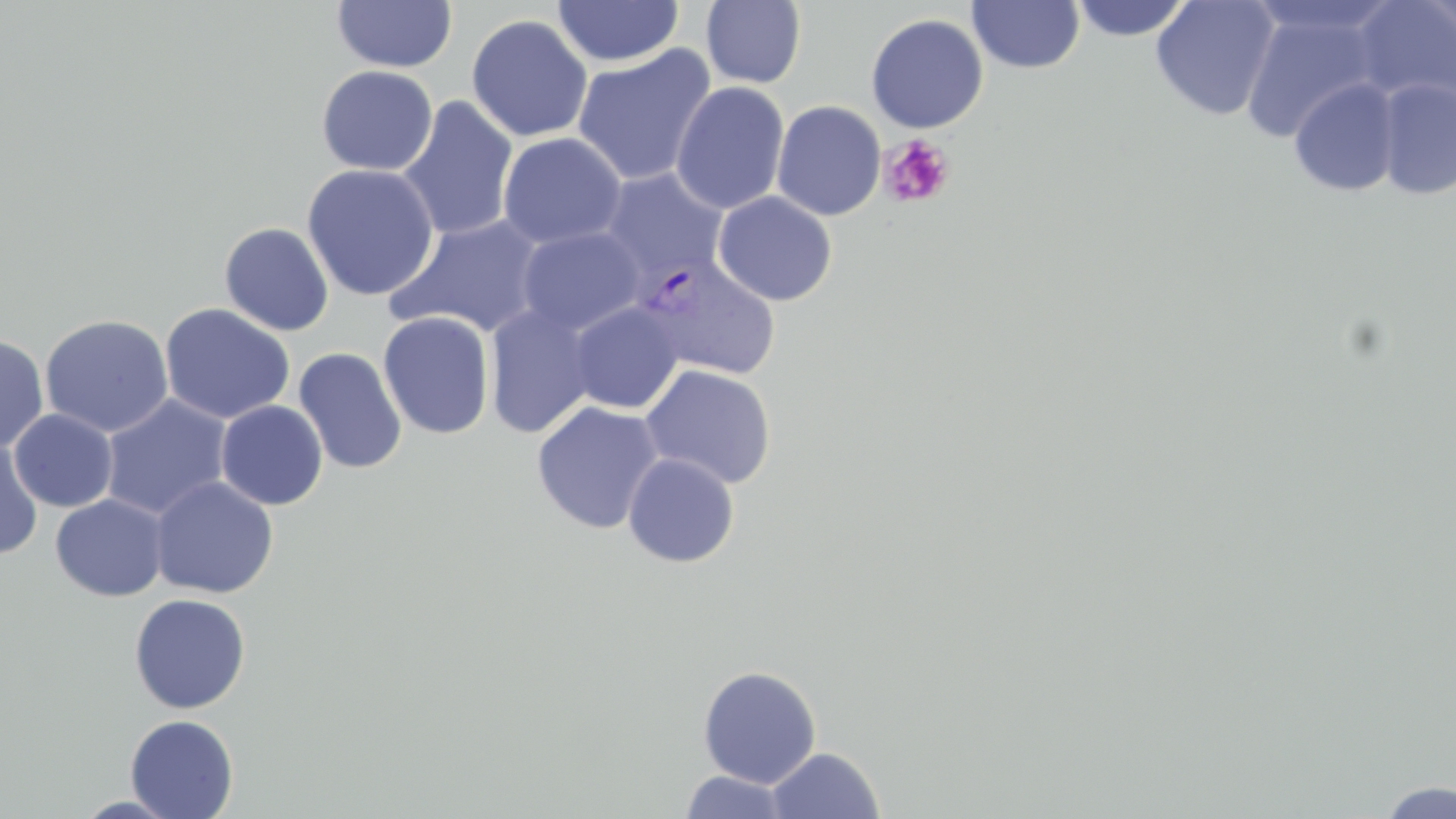

Summary:
  - Coordinate format: approximate bounding boxes as [x1, y1, x2, y2] in pixels
  - Uninfected red blood cell locations: [331, 0, 457, 73], [1069, 0, 1193, 42], [1151, 0, 1280, 121], [1351, 0, 1456, 113], [552, 1, 684, 68], [701, 1, 806, 89], [967, 1, 1085, 75], [1239, 6, 1387, 142], [866, 13, 989, 134], [466, 14, 593, 143], [572, 44, 718, 186], [316, 65, 438, 176], [1288, 77, 1401, 199], [1375, 77, 1456, 200], [670, 81, 790, 215], [396, 96, 519, 242], [772, 100, 886, 221], [498, 132, 627, 250], [301, 163, 440, 301], [598, 168, 729, 287], [712, 191, 838, 306], [387, 214, 547, 338], [219, 222, 334, 336], [516, 227, 646, 338], [567, 302, 684, 414], [159, 303, 295, 425], [484, 303, 598, 439], [378, 311, 495, 440], [39, 313, 175, 438], [0, 336, 49, 454], [294, 347, 407, 474], [640, 364, 777, 490], [100, 395, 233, 521], [215, 400, 328, 510], [531, 401, 666, 535], [9, 408, 118, 512], [0, 438, 43, 560], [622, 452, 740, 568], [140, 475, 263, 711], [149, 476, 279, 599], [50, 494, 169, 601], [128, 593, 251, 714], [697, 664, 822, 789], [125, 715, 239, 818], [766, 746, 884, 818], [678, 770, 793, 818], [1376, 778, 1455, 818], [72, 795, 184, 818]
  - Plasmodium vivax-infected red blood cell locations: [633, 253, 782, 382]
  - Platelet locations: [879, 135, 955, 209]
  - Slide-level diagnosis: Plasmodium vivax
  - Image size: 1456×819 pixels
  - Magnification: 1000x
  - Preparation: thin blood film
  - Modality: optical microscopy
  - Stain: May-Grünwald-Giemsa
  - Field of view: single